Describe the morphology of the erythrocytes.
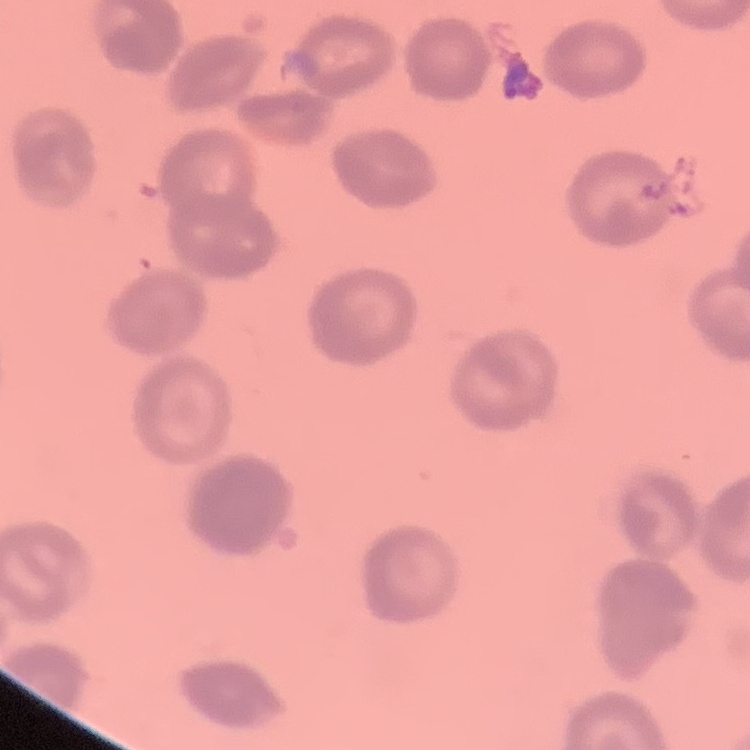

Rouleaux formation.

Thin peripheral smear. Square crop of a larger photomicrograph. Field's or Giemsa stain.